Name the blood parasite species.
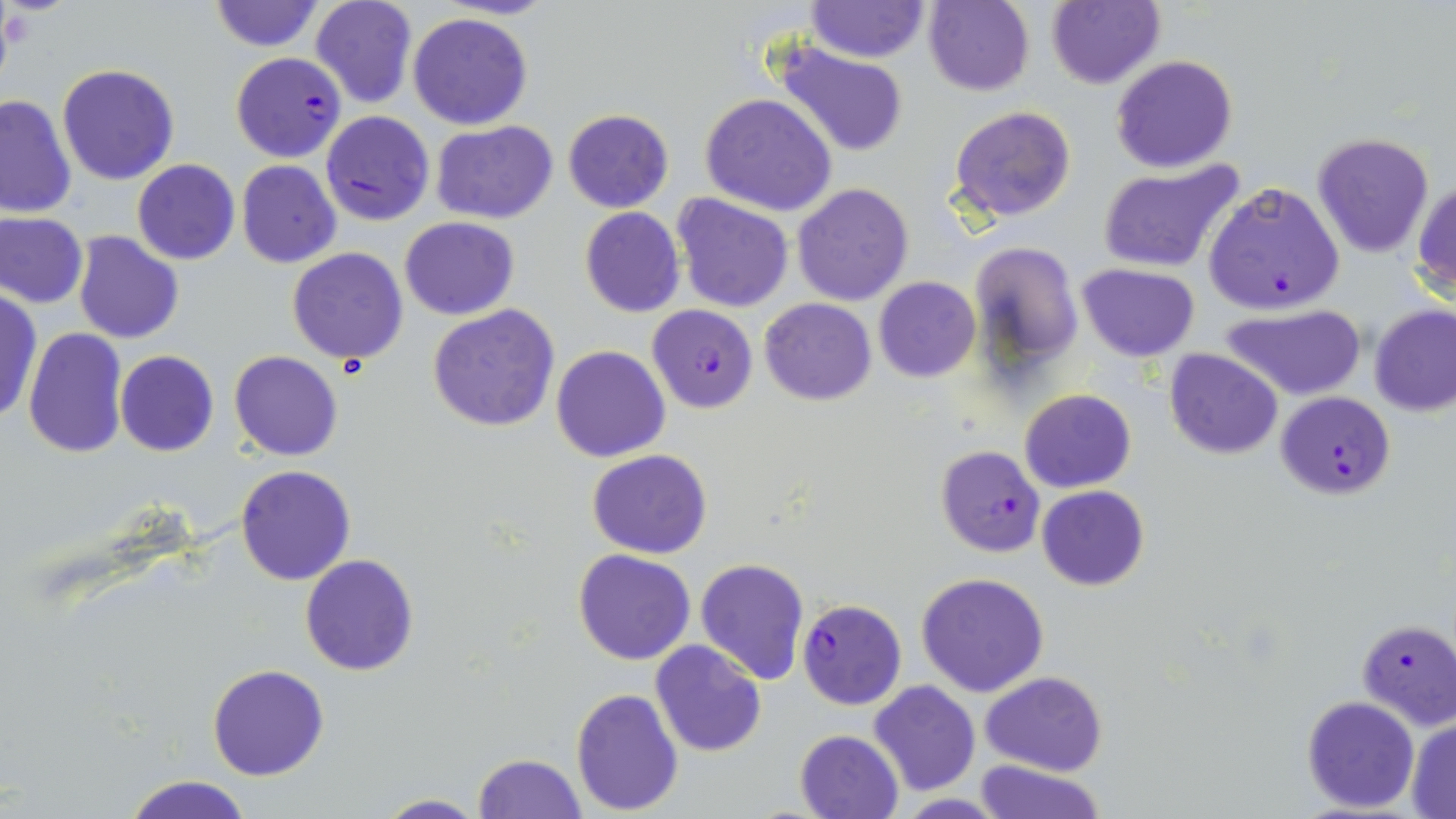
Plasmodium falciparum.

uninfected red blood cell locations = approximate bounding boxes as named x1/y1/x2/y2 corners in pixels: (x1=208, y1=0, x2=325, y2=53), (x1=311, y1=0, x2=418, y2=109), (x1=436, y1=0, x2=558, y2=20), (x1=923, y1=0, x2=1034, y2=97), (x1=1045, y1=0, x2=1164, y2=90), (x1=805, y1=1, x2=930, y2=64), (x1=407, y1=11, x2=533, y2=130), (x1=767, y1=40, x2=911, y2=160), (x1=1110, y1=54, x2=1238, y2=173), (x1=57, y1=64, x2=180, y2=185), (x1=0, y1=93, x2=75, y2=217), (x1=699, y1=93, x2=838, y2=217), (x1=948, y1=105, x2=1077, y2=224), (x1=562, y1=108, x2=674, y2=212), (x1=432, y1=120, x2=557, y2=225), (x1=1311, y1=132, x2=1434, y2=257), (x1=132, y1=159, x2=239, y2=265), (x1=236, y1=160, x2=342, y2=268), (x1=1095, y1=161, x2=1245, y2=273), (x1=1413, y1=178, x2=1456, y2=299), (x1=791, y1=183, x2=914, y2=306), (x1=672, y1=192, x2=795, y2=313), (x1=579, y1=207, x2=685, y2=317), (x1=1, y1=212, x2=87, y2=308), (x1=399, y1=217, x2=519, y2=320), (x1=75, y1=231, x2=185, y2=344), (x1=971, y1=240, x2=1084, y2=379), (x1=287, y1=247, x2=411, y2=364), (x1=1077, y1=262, x2=1199, y2=361), (x1=872, y1=277, x2=981, y2=382), (x1=1, y1=289, x2=41, y2=425), (x1=760, y1=297, x2=876, y2=406), (x1=427, y1=303, x2=560, y2=432), (x1=1370, y1=303, x2=1456, y2=416), (x1=1224, y1=304, x2=1366, y2=401), (x1=22, y1=328, x2=129, y2=458), (x1=551, y1=345, x2=671, y2=463), (x1=1164, y1=347, x2=1284, y2=459), (x1=115, y1=350, x2=220, y2=457), (x1=230, y1=351, x2=341, y2=460), (x1=1019, y1=388, x2=1137, y2=493), (x1=587, y1=450, x2=713, y2=559), (x1=236, y1=464, x2=356, y2=585), (x1=1036, y1=484, x2=1149, y2=591), (x1=572, y1=548, x2=696, y2=665), (x1=300, y1=554, x2=420, y2=676), (x1=695, y1=557, x2=810, y2=685), (x1=916, y1=571, x2=1050, y2=698), (x1=650, y1=640, x2=766, y2=757), (x1=207, y1=664, x2=330, y2=781), (x1=981, y1=671, x2=1107, y2=776), (x1=868, y1=680, x2=981, y2=796), (x1=571, y1=688, x2=683, y2=812), (x1=1301, y1=695, x2=1419, y2=812), (x1=1406, y1=718, x2=1456, y2=817), (x1=795, y1=729, x2=905, y2=819), (x1=472, y1=753, x2=586, y2=819), (x1=974, y1=758, x2=1106, y2=819), (x1=123, y1=774, x2=254, y2=818), (x1=373, y1=794, x2=486, y2=818)
modality = optical microscopy
Plasmodium falciparum-infected red blood cell locations = approximate bounding boxes as named x1/y1/x2/y2 corners in pixels: (x1=231, y1=52, x2=346, y2=162), (x1=319, y1=110, x2=434, y2=227), (x1=1204, y1=182, x2=1345, y2=314), (x1=647, y1=304, x2=756, y2=413), (x1=1275, y1=392, x2=1396, y2=498), (x1=934, y1=445, x2=1046, y2=557), (x1=797, y1=599, x2=906, y2=710), (x1=1356, y1=619, x2=1456, y2=727)
preparation = thin blood film
magnification = 1000x
field of view = one of a larger specimen
stain = May-Grünwald-Giemsa
image size = 1456×819 pixels